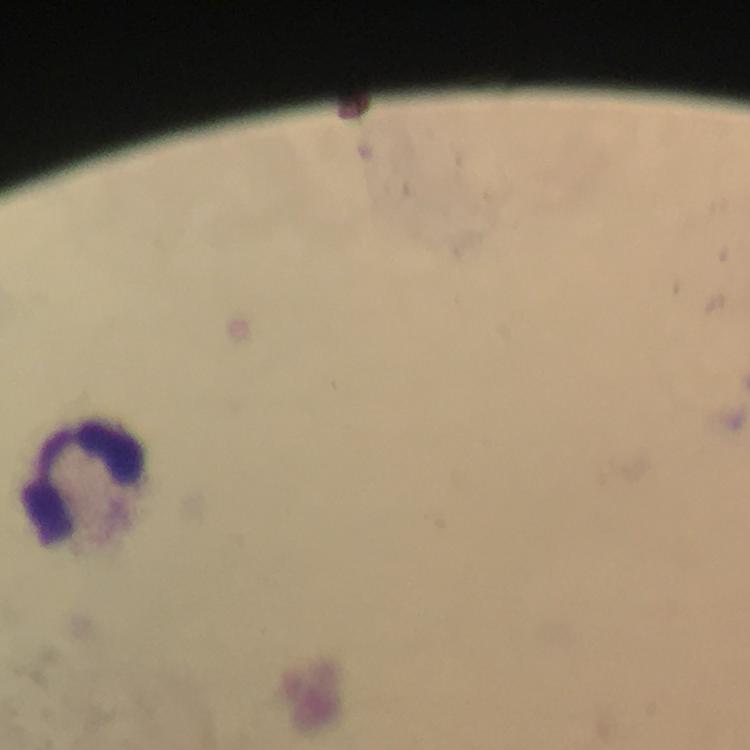

{
  "capture": "smartphone mounted on the microscope",
  "preparation": "thick blood film",
  "immersion_oil": "applied",
  "magnification": "100x",
  "stain": "Giemsa",
  "leukocyte_locations": "approximate centers as [x, y] in pixels: [82, 484]",
  "context": "from a diagnostic examination for malaria",
  "image_size": "750×750 pixels",
  "cropped_from": "a single field of view",
  "plasmodium_parasites": "none detected"
}